Give the position of every leukocyte visible.
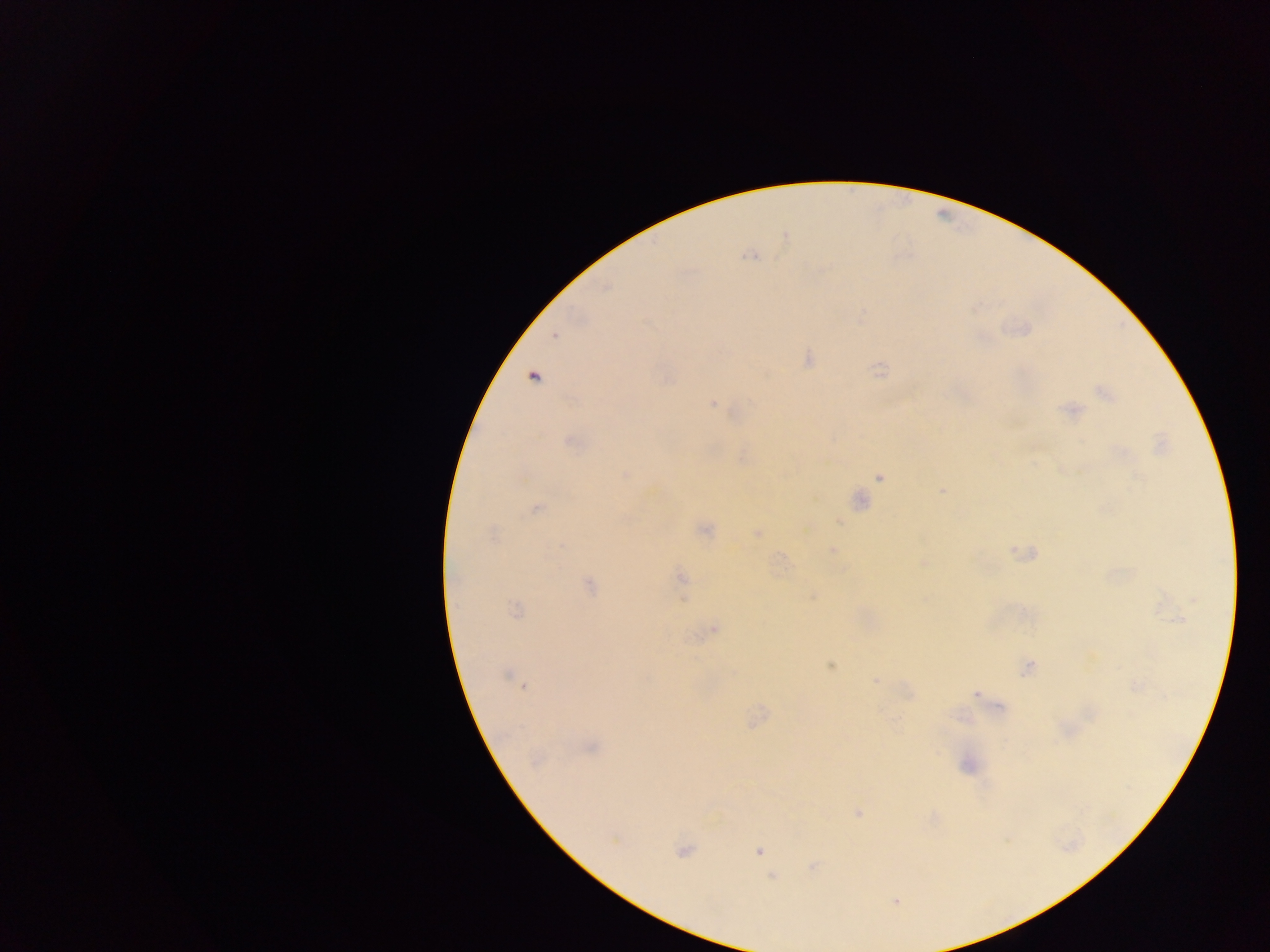

No leukocytes observed.

image size = 1270×952 pixels
malaria parasite locations = approximate centers as {x, y} in pixels: {750, 256}, {555, 336}, {808, 359}, {534, 378}, {667, 379}, {1105, 393}, {713, 404}, {1071, 411}, {571, 443}, {622, 475}, {879, 477}, {941, 491}, {859, 501}, {536, 508}, {705, 530}, {757, 533}, {493, 535}, {832, 550}, {923, 563}, {681, 578}, {589, 585}, {812, 596}, {515, 610}, {1178, 620}, {715, 628}, {830, 666}, {1028, 667}, {506, 675}, {875, 681}, {523, 687}, {976, 695}, {999, 706}, {592, 747}, {535, 761}, {859, 812}, {613, 842}, {758, 850}, {682, 851}, {812, 866}, {773, 877}, {896, 901}
preparation = thick blood smear
country = Ghana
field of view = single
capture = mobile-phone photograph through a microscope